Report the malaria status of this cell.
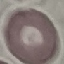

Uninfected.

Summary:
  - Capture: smartphone camera at the microscope eyepiece
  - Image type: cell patch, automatically extracted from a larger field of view and resized to 64 × 64 pixels
  - Stain: Giemsa
  - Preparation: thin blood film